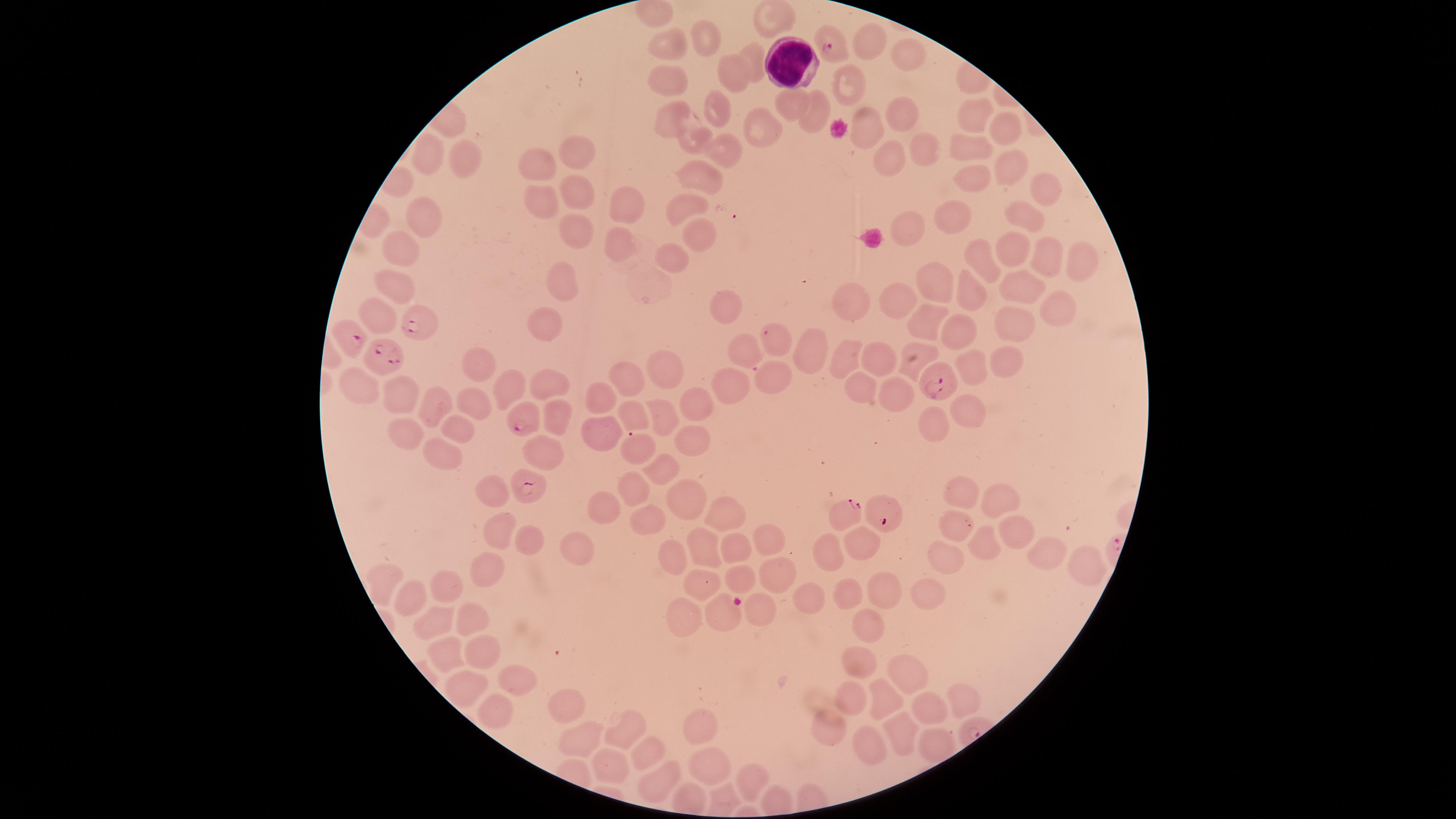 Approximate marker points as [x, y] in pixels. Parasitized red blood cells: [832, 44], [417, 323], [381, 355], [937, 382], [522, 421], [633, 443], [528, 485], [842, 514], [884, 516]. White blood cells: [792, 63]. Uninfected red blood cells: [773, 18], [877, 35], [703, 40], [664, 45], [907, 53], [754, 57], [733, 75], [666, 77], [847, 84], [787, 103], [717, 111], [818, 114], [899, 114], [973, 114], [673, 117], [871, 129], [1003, 129], [758, 132], [689, 137], [925, 143], [973, 146], [428, 150], [576, 153], [723, 153], [465, 161], [536, 163], [888, 163], [1011, 164], [697, 175], [970, 178], [1039, 188], [578, 189], [541, 197], [627, 202], [687, 205], [1021, 213], [425, 215], [960, 221], [577, 226], [905, 229], [697, 230], [620, 237], [1011, 244], [401, 248], [1086, 254], [676, 258], [1044, 258], [982, 259], [564, 281], [396, 282], [942, 283], [1021, 285], [973, 296], [898, 298], [856, 302], [731, 305], [1060, 306], [377, 316], [543, 322], [929, 322], [1014, 326], [961, 332], [775, 342], [745, 351], [814, 351], [846, 356], [916, 356], [1003, 357], [879, 360], [479, 365], [671, 367], [971, 368], [773, 375], [624, 377], [859, 381], [512, 386], [549, 387], [360, 388], [727, 389], [601, 392], [894, 392], [398, 394], [696, 402], [470, 404], [432, 406], [967, 407], [632, 408], [658, 409], [553, 422], [931, 422], [600, 426], [455, 429], [404, 434], [692, 439], [543, 449], [442, 450], [660, 469], [637, 486], [488, 490], [963, 494], [1000, 497], [680, 500], [608, 505], [726, 514], [646, 520], [492, 526], [955, 527], [1021, 533], [523, 537], [769, 543], [980, 543], [572, 546], [865, 546], [737, 548], [699, 549], [829, 550], [1045, 552], [943, 559], [674, 560], [1081, 560], [484, 566], [741, 578], [774, 579], [696, 582], [386, 584], [449, 587], [846, 592], [881, 592], [924, 592], [410, 595], [802, 601], [756, 610], [721, 614], [435, 617], [469, 617], [680, 618], [863, 631], [481, 648], [446, 653], [856, 659], [905, 671], [511, 673], [471, 688], [853, 693], [885, 694], [959, 703], [498, 706], [570, 708], [929, 712], [697, 724], [829, 727], [626, 731], [897, 737], [584, 741], [867, 743], [932, 746], [646, 751], [705, 761], [614, 767], [658, 779], [749, 781]. Giemsa-stained preparation. Image is 1456×819 pixels. Thin smear of blood. The visible region is circular. Photographed with a smartphone camera through the microscope eyepiece. Species: Plasmodium falciparum. Presence: malaria parasites identified. Single field of view.